State the blood parasite species.
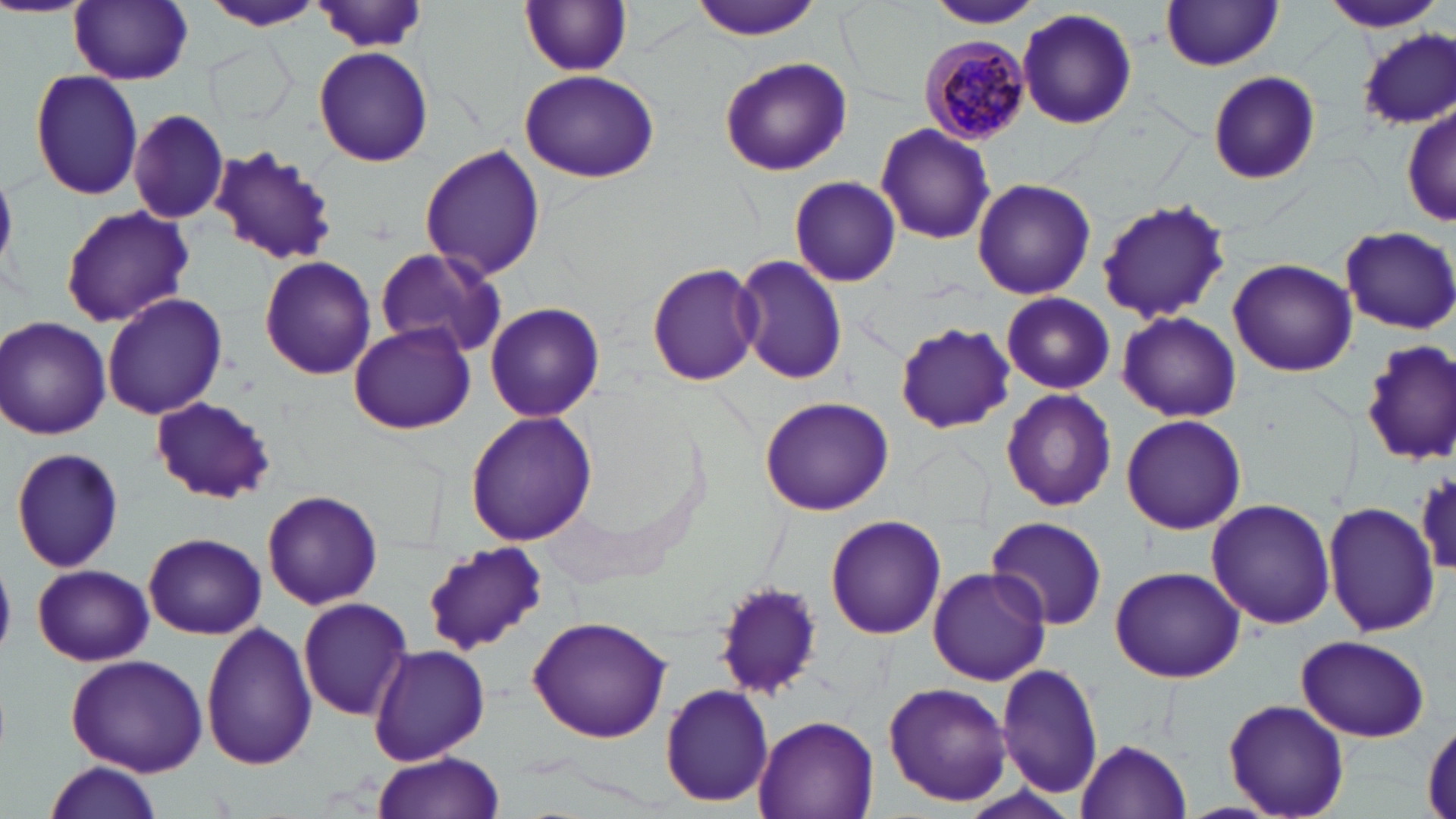

Plasmodium malariae.

Approximate bounding boxes as [x1, y1, x2, y2] in pixels. Plasmodium malariae-infected red blood cell locations: [919, 34, 1032, 147]. Uninfected red blood cell locations: [204, 0, 325, 33], [689, 0, 822, 39], [924, 0, 1046, 29], [1319, 0, 1445, 34], [69, 1, 193, 85], [520, 2, 632, 77], [1162, 2, 1284, 71], [314, 4, 432, 52], [1017, 7, 1138, 133], [1359, 30, 1455, 132], [209, 42, 293, 127], [313, 48, 434, 166], [718, 58, 852, 177], [28, 68, 144, 199], [519, 69, 660, 184], [1207, 71, 1320, 185], [1402, 101, 1454, 232], [128, 108, 230, 224], [875, 122, 997, 246], [210, 146, 335, 267], [417, 146, 547, 282], [788, 175, 902, 287], [970, 177, 1095, 299], [1093, 198, 1234, 322], [61, 206, 195, 325], [1339, 224, 1456, 334], [372, 247, 508, 361], [733, 253, 845, 387], [260, 255, 375, 379], [1228, 258, 1356, 377], [647, 262, 764, 386], [101, 291, 227, 420], [1001, 293, 1117, 395], [484, 301, 604, 423], [1118, 311, 1241, 422], [1, 316, 111, 440], [895, 321, 1017, 432], [347, 322, 476, 435], [1358, 338, 1456, 467], [999, 389, 1117, 512], [759, 395, 894, 516], [149, 397, 275, 504], [464, 411, 598, 545], [1120, 414, 1246, 536], [9, 446, 125, 575], [1415, 468, 1456, 580], [262, 489, 383, 610], [1206, 497, 1336, 630], [1324, 500, 1439, 638], [987, 514, 1108, 630], [823, 515, 946, 640], [143, 532, 265, 639], [420, 542, 547, 655], [32, 564, 153, 666], [1109, 566, 1244, 682], [926, 567, 1052, 685], [714, 579, 826, 699], [296, 597, 411, 721], [528, 614, 673, 743], [200, 622, 319, 771], [1296, 634, 1430, 742], [369, 642, 490, 765], [64, 651, 209, 776], [996, 663, 1104, 798], [882, 682, 1013, 809], [660, 683, 774, 808], [1223, 699, 1350, 819], [752, 713, 879, 819], [1424, 723, 1456, 816], [1075, 738, 1192, 818], [371, 753, 505, 819], [42, 761, 163, 819]. Image is 1456×819 pixels. Light microscopy. Thin blood smear. 1000x magnification. May-Grünwald-Giemsa stain. One field of a larger specimen.